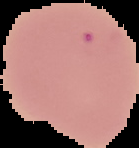

Summary:
  - Preparation: thin blood smear
  - Image size: 139×148 pixels
  - Malaria status: uninfected
  - Image type: cell region segmented out of the field of view; surrounding area masked to black